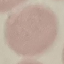
malaria status = uninfected
stain = Giemsa
preparation = thin smear
capture = smartphone through the microscope eyepiece
image type = automatically extracted cell patch, resized to 64 × 64 pixels